Find the cells and give the type of each one.
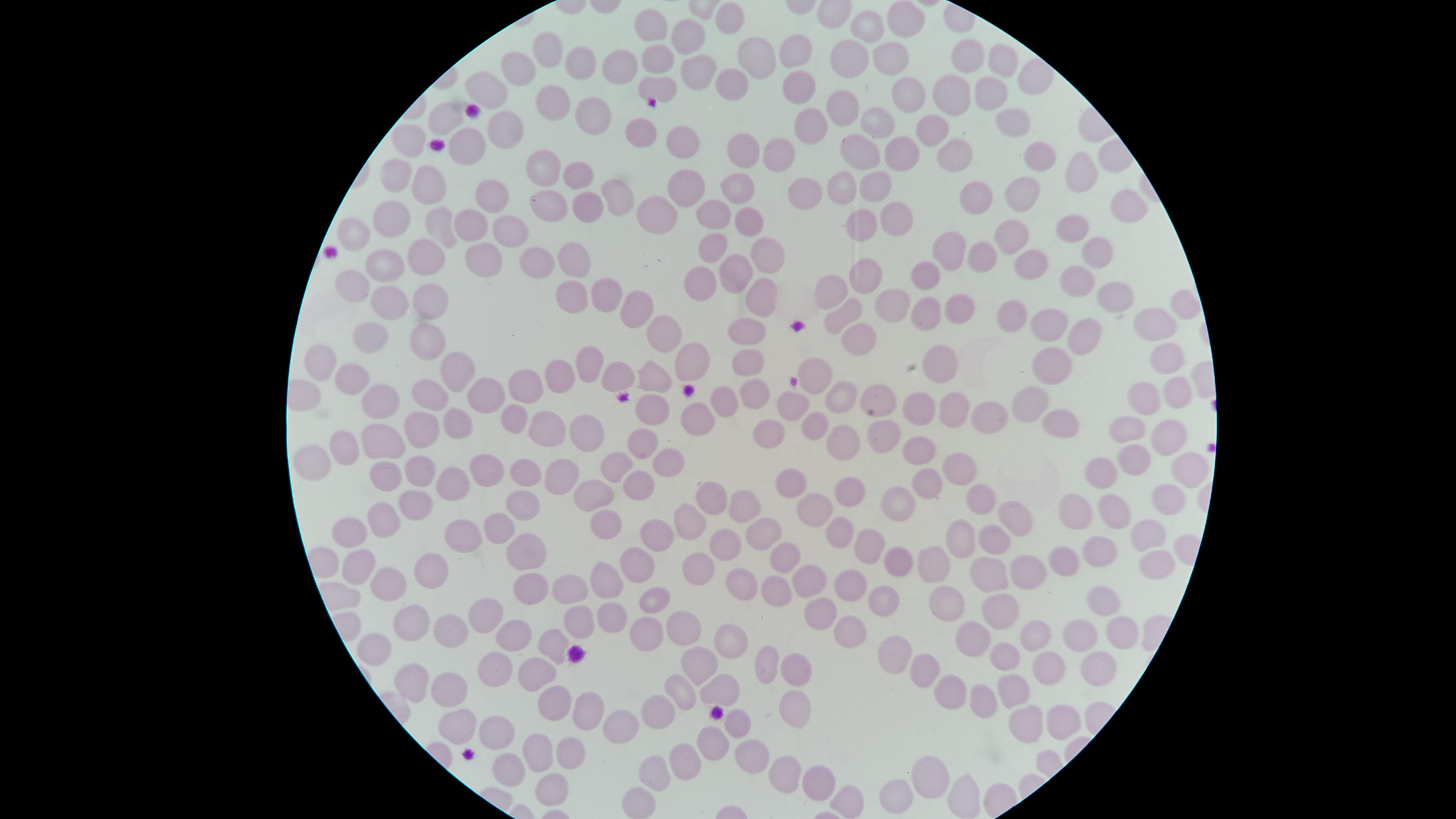

No parasitized RBCs identified.
Approximate marker points as [x, y] in pixels.
Uninfected RBCs: [728, 15], [902, 18], [650, 24], [860, 27], [690, 35], [551, 48], [794, 49], [840, 52], [751, 57], [581, 58], [650, 58], [887, 59], [968, 59], [617, 61], [1000, 67], [515, 70], [701, 70], [1033, 75], [724, 78], [790, 83], [484, 85], [647, 85], [953, 86], [989, 86], [905, 90], [847, 105], [548, 106], [444, 114], [813, 119], [600, 120], [871, 121], [923, 121], [505, 127], [1015, 128], [647, 131], [407, 138], [682, 144], [468, 145], [739, 146], [858, 147], [949, 149], [1038, 150], [899, 151], [773, 154], [546, 166], [578, 170], [394, 173], [1071, 176], [735, 186], [843, 186], [427, 188], [866, 188], [804, 189], [985, 190], [1030, 190], [689, 191], [617, 196], [489, 198], [547, 200], [589, 206], [652, 206], [709, 211], [892, 212], [1119, 212], [467, 216], [395, 218], [860, 220], [748, 223], [508, 227], [1074, 228], [441, 229], [355, 232], [1007, 234], [946, 245], [710, 249], [764, 251], [1093, 252], [424, 253], [477, 253], [981, 254], [571, 255], [1034, 257], [525, 261], [381, 264], [732, 272], [858, 274], [929, 275], [347, 279], [695, 280], [1082, 280], [834, 286], [606, 288], [433, 289], [577, 289], [1118, 293], [755, 295], [887, 297], [394, 302], [1187, 304], [969, 307], [621, 308], [1013, 309], [922, 312], [840, 315], [1050, 318], [1148, 319], [659, 330], [1083, 330], [745, 332], [372, 334], [851, 334], [425, 338], [748, 355], [692, 356], [323, 358], [1173, 358], [937, 362], [590, 366], [1046, 367], [453, 369], [655, 371], [818, 373], [558, 374], [619, 376], [348, 381], [527, 386], [752, 387], [719, 391], [431, 394], [878, 394], [845, 395], [1172, 395], [476, 397], [1033, 397], [375, 400], [1138, 400], [642, 403], [794, 403], [923, 405], [959, 411], [989, 413], [689, 415], [1059, 417], [447, 419], [811, 422], [414, 423], [511, 424], [549, 429], [768, 429], [1133, 430], [584, 433], [877, 433], [1169, 433], [377, 439], [633, 439], [843, 443], [917, 446], [341, 447], [311, 457], [659, 457], [1135, 459], [486, 463], [608, 465], [958, 465], [417, 466], [1185, 466], [559, 467], [1107, 474], [388, 475], [525, 475], [462, 478], [634, 479], [929, 482], [789, 485], [853, 488], [591, 493], [710, 495], [893, 499], [740, 500], [979, 500], [419, 502], [1075, 504], [1165, 505], [513, 506], [1115, 506], [816, 511], [1015, 511], [602, 517], [384, 521], [688, 522], [461, 525], [755, 525], [495, 527], [845, 531], [1148, 532], [345, 533], [664, 534], [959, 536], [997, 541], [721, 543], [864, 545], [518, 549], [1104, 549], [784, 550], [1070, 557], [895, 558], [354, 564], [641, 564], [1148, 565], [699, 566], [423, 567], [928, 569], [602, 575], [993, 576], [1033, 576], [743, 578], [386, 580], [804, 582], [847, 586], [527, 587], [779, 588], [568, 592], [653, 594], [1100, 599], [941, 602], [878, 603], [820, 606], [487, 607], [607, 607], [414, 615], [1001, 615], [678, 616], [572, 623], [648, 628], [844, 631], [1115, 631], [447, 632], [509, 632], [1077, 633], [1033, 635], [968, 639], [376, 640], [550, 640], [726, 640], [1010, 650], [895, 653], [698, 659], [491, 660], [1052, 660], [532, 663], [769, 664], [917, 665], [802, 666], [1094, 670], [411, 678], [1015, 682], [941, 685], [720, 687], [446, 688], [678, 688], [547, 692], [981, 700], [577, 706], [459, 712], [793, 712], [663, 716], [1055, 717], [1023, 721], [736, 723], [621, 725], [498, 727], [713, 738], [567, 739], [747, 748], [540, 751], [688, 754], [652, 763], [925, 768], [511, 771], [781, 773], [807, 774], [547, 782], [898, 793], [966, 796], [632, 798], [846, 799].
No WBCs identified.

stain = Giemsa
preparation = thin blood film
visible region = circular
field of view = single
capture = smartphone photograph through the microscope eyepiece
image size = 1456×819 pixels